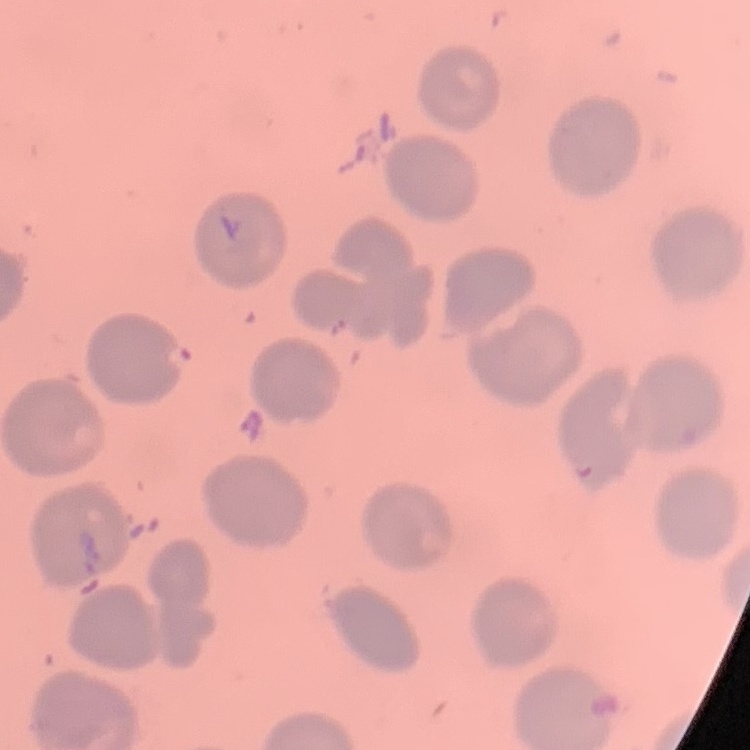

red blood cell morphology = no rouleaux formation
preparation = thin blood film
image type = square crop of a larger photomicrograph
stain = Field's or Giemsa